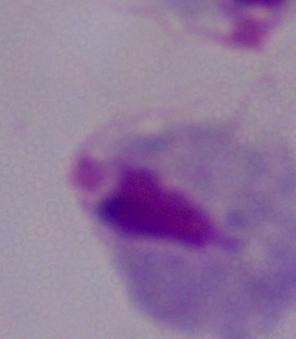

identification = trichomonad
modality = photomicrograph
magnification = 1000x